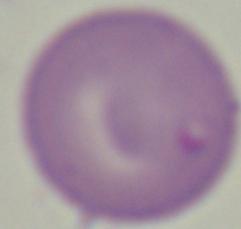
modality = micrograph
identification = Babesia
magnification = 1000x